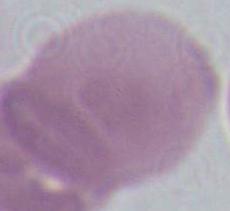
Summary:
  - Magnification: 1000x
  - Identification: red blood cell
  - Modality: micrograph